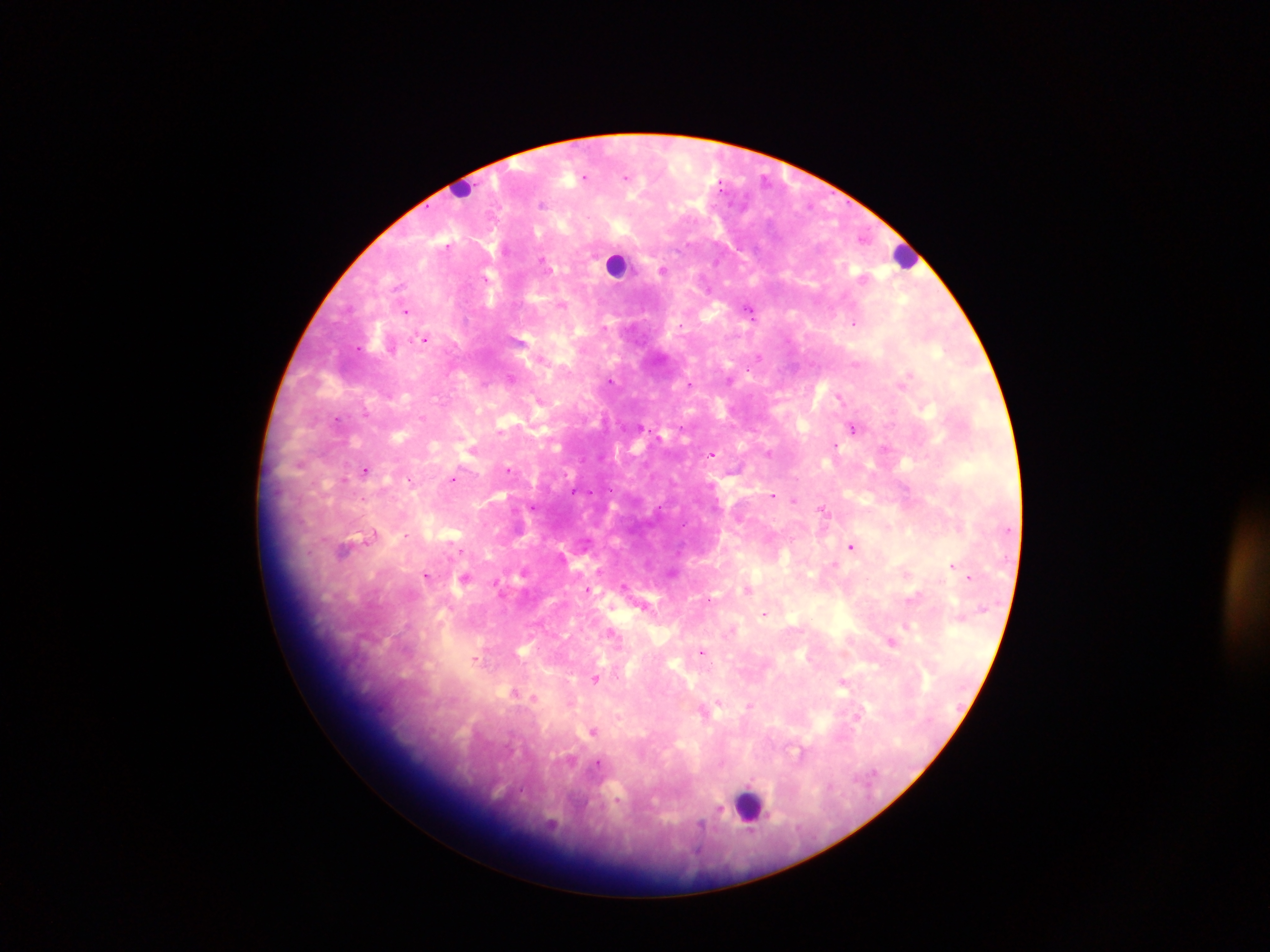

Approximate centers as {x, y} in pixels. Leukocyte locations: {462, 185}, {905, 255}, {616, 264}, {750, 805}. Malaria parasite locations: {626, 176}, {584, 177}, {542, 204}, {447, 247}, {544, 262}, {663, 271}, {563, 305}, {406, 311}, {750, 311}, {855, 323}, {604, 328}, {425, 339}, {358, 348}, {759, 357}, {909, 376}, {510, 378}, {611, 380}, {690, 383}, {483, 384}, {839, 397}, {365, 413}, {336, 419}, {641, 427}, {680, 427}, {853, 427}, {500, 431}, {835, 444}, {884, 447}, {769, 452}, {712, 454}, {365, 470}, {509, 470}, {452, 479}, {343, 480}, {411, 480}, {573, 491}, {773, 495}, {794, 500}, {533, 507}, {659, 508}, {822, 510}, {407, 535}, {372, 536}, {851, 546}, {345, 548}, {461, 551}, {952, 566}, {427, 575}, {969, 577}, {465, 578}, {624, 586}, {588, 590}, {747, 590}, {913, 597}, {709, 599}, {764, 614}, {906, 626}, {612, 633}, {892, 642}, {701, 652}, {476, 659}, {596, 678}, {842, 682}, {514, 693}, {533, 698}, {749, 705}, {704, 712}, {856, 717}, {594, 731}, {597, 765}, {718, 811}, {700, 826}. Thick blood film. Collected in Ghana. Mobile-phone photograph taken through the microscope. One field of view. Image is 1270×952 pixels.